Give the position of every leukocyte.
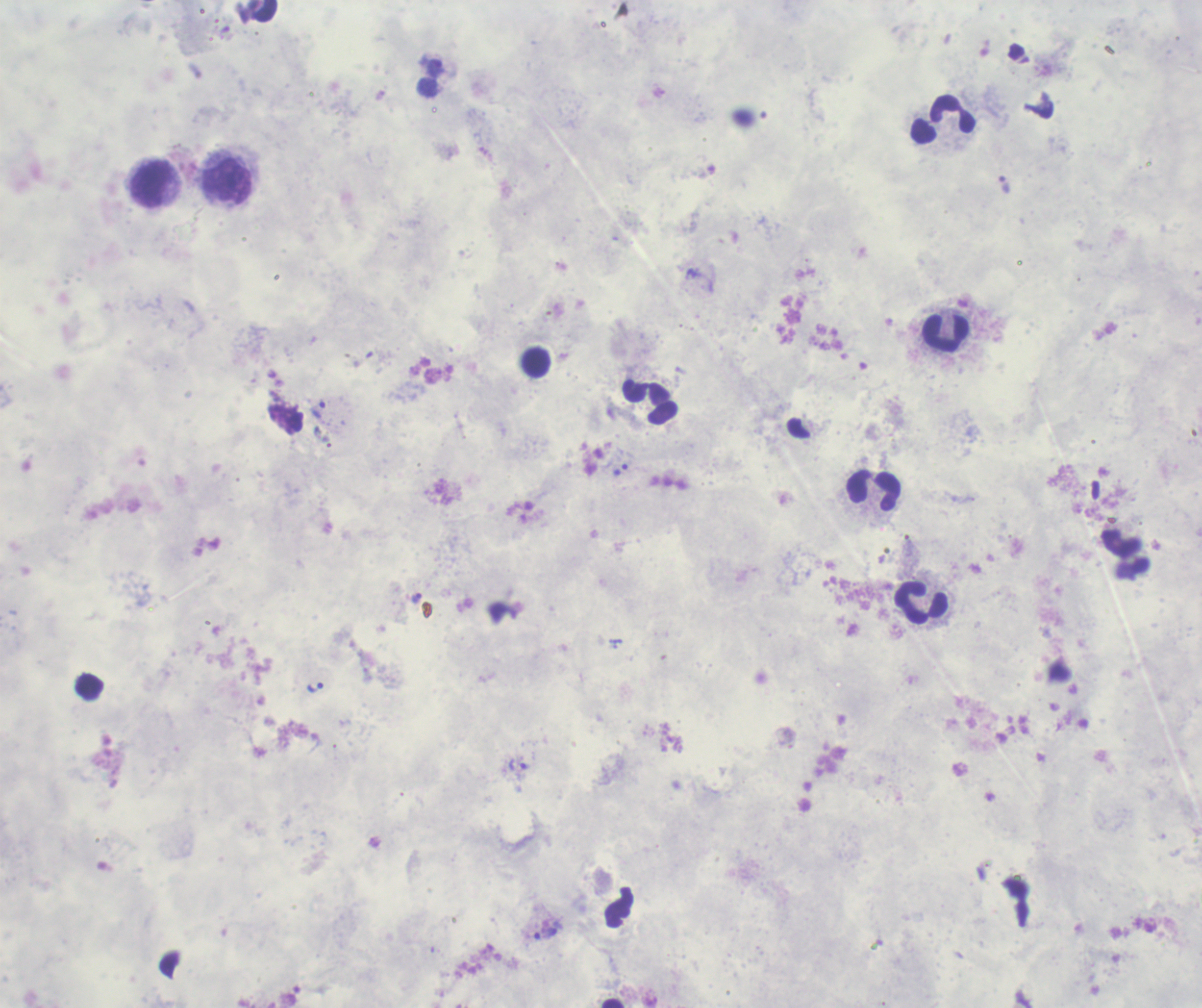

Approximate object centers, in pixels from the top-left corner.
Leukocytes: (x=942, y=120), (x=228, y=180), (x=149, y=185), (x=946, y=333), (x=650, y=402), (x=874, y=491), (x=921, y=603).

Approximate object centers, in pixels from the top-left corner. Trophozoite locations: (x=1004, y=185), (x=319, y=411), (x=621, y=470), (x=417, y=598), (x=314, y=687), (x=517, y=764), (x=546, y=934). Thick blood smear. 100x magnification. Romanowsky-stained preparation. Result: malaria parasites detected. Background quality: unsatisfactory. Image is 1202×1008 pixels. Single field of view. Previously used in a real diagnosis.